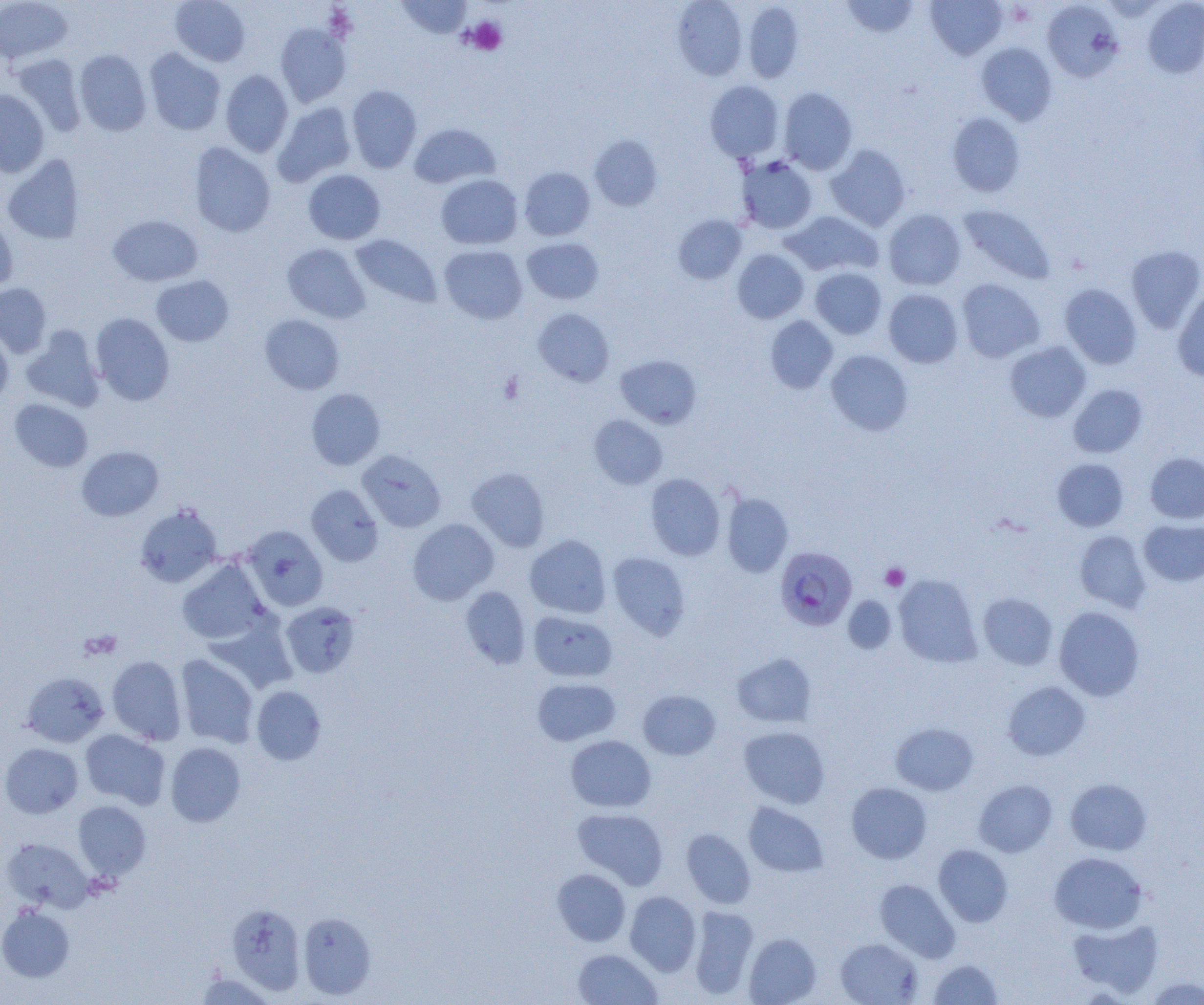
Approximate bounding boxes as (x1,y1)-(x2,y2) corner pairs in pixels. Platelet locations: (465,17)-(507,55), (881,563)-(909,590), (80,630)-(122,660). Plasmodium falciparum-infected red blood cell locations: (775,546)-(857,631). Uninfected red blood cell locations: (170,0)-(251,66), (397,0)-(472,39), (672,0)-(747,80), (841,0)-(918,37), (926,0)-(1007,60), (1143,0)-(1204,78), (0,1)-(72,64), (1042,1)-(1123,82), (743,2)-(804,83), (275,23)-(351,107), (976,42)-(1057,125), (144,48)-(225,135), (74,49)-(151,135), (13,53)-(87,137), (220,70)-(293,157), (705,80)-(784,162), (347,85)-(422,173), (778,87)-(858,174), (0,90)-(50,177), (273,102)-(356,187), (947,112)-(1025,197), (409,123)-(500,189), (589,135)-(663,211), (189,143)-(276,237), (825,144)-(910,231), (2,154)-(86,244), (737,156)-(818,234), (520,166)-(595,241), (304,169)-(385,245), (436,174)-(522,249), (958,204)-(1056,285), (883,209)-(966,290), (782,211)-(883,277), (0,214)-(18,292), (108,215)-(203,286), (673,215)-(747,284), (351,234)-(441,308), (522,238)-(604,304), (282,243)-(370,323), (439,245)-(527,324), (1126,245)-(1204,333), (732,249)-(809,324), (810,267)-(887,339), (151,275)-(234,347), (957,278)-(1045,362), (0,283)-(51,358), (1059,284)-(1141,369), (1173,287)-(1204,381), (883,289)-(963,368), (533,308)-(614,387), (91,313)-(175,404), (259,314)-(345,395), (765,316)-(838,393), (21,327)-(105,412), (0,329)-(13,405), (1005,341)-(1091,422), (826,349)-(913,435), (615,354)-(702,429), (1068,384)-(1147,458), (306,388)-(385,470), (9,398)-(93,472), (589,415)-(667,489), (77,446)-(164,521), (358,450)-(446,532), (1145,453)-(1204,523), (1052,458)-(1128,531), (467,467)-(550,552), (645,473)-(725,561), (306,484)-(384,566), (721,493)-(793,578), (135,504)-(223,587), (407,518)-(499,605), (1139,519)-(1204,586), (242,525)-(328,611), (1074,530)-(1151,612), (525,535)-(611,618), (607,552)-(690,640), (177,559)-(268,645), (894,574)-(982,667), (461,586)-(531,669), (978,592)-(1057,670), (843,596)-(896,655), (281,602)-(361,678), (1054,606)-(1145,701), (528,610)-(617,682), (732,653)-(817,728), (107,655)-(187,745), (175,655)-(258,748), (21,672)-(109,747), (532,678)-(620,746), (1002,681)-(1090,760), (251,685)-(326,765), (638,690)-(721,760), (890,722)-(978,796), (739,726)-(830,808), (80,729)-(170,809), (565,735)-(656,812), (165,742)-(246,827), (0,743)-(83,818), (1065,778)-(1152,855), (974,779)-(1057,857), (846,782)-(932,864), (73,800)-(151,880), (743,802)-(829,877), (573,808)-(668,889), (681,828)-(756,908), (2,837)-(95,912), (933,844)-(1013,927), (1049,852)-(1148,934), (552,869)-(630,946), (875,879)-(960,962), (625,891)-(701,976), (227,903)-(306,994), (0,905)-(74,981), (689,906)-(759,999), (299,912)-(376,999), (1068,917)-(1164,998), (744,933)-(821,1004), (835,937)-(922,1005), (573,949)-(661,1004), (928,959)-(1003,1004), (194,971)-(274,1004), (1144,976)-(1203,1004). Slide-level diagnosis: Plasmodium falciparum. One field of a larger specimen. Image is 1204×1005 pixels. Captured at 1000x magnification. Thin blood film. Optical microscopy.